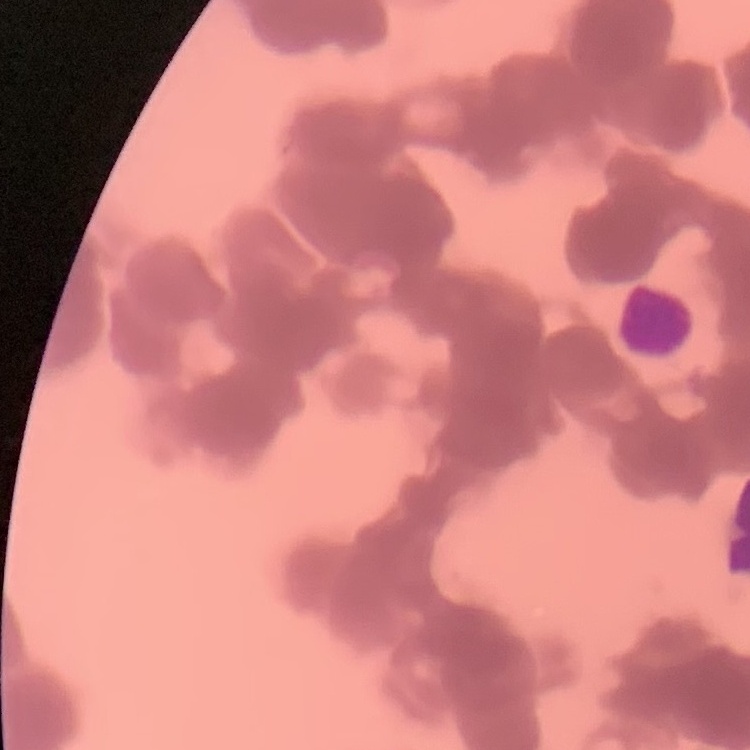

Summary:
  - Erythrocyte morphology: rouleaux formation
  - Preparation: thin blood film
  - Image type: square crop of a larger photomicrograph
  - Stain: Field's or Giemsa